Assess this cell for malaria.
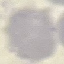

Uninfected.

Summary:
  - Image type: automatically extracted cell patch, resized to 64 × 64 pixels
  - Stain: Giemsa
  - Capture: smartphone camera at the microscope eyepiece
  - Preparation: thin smear